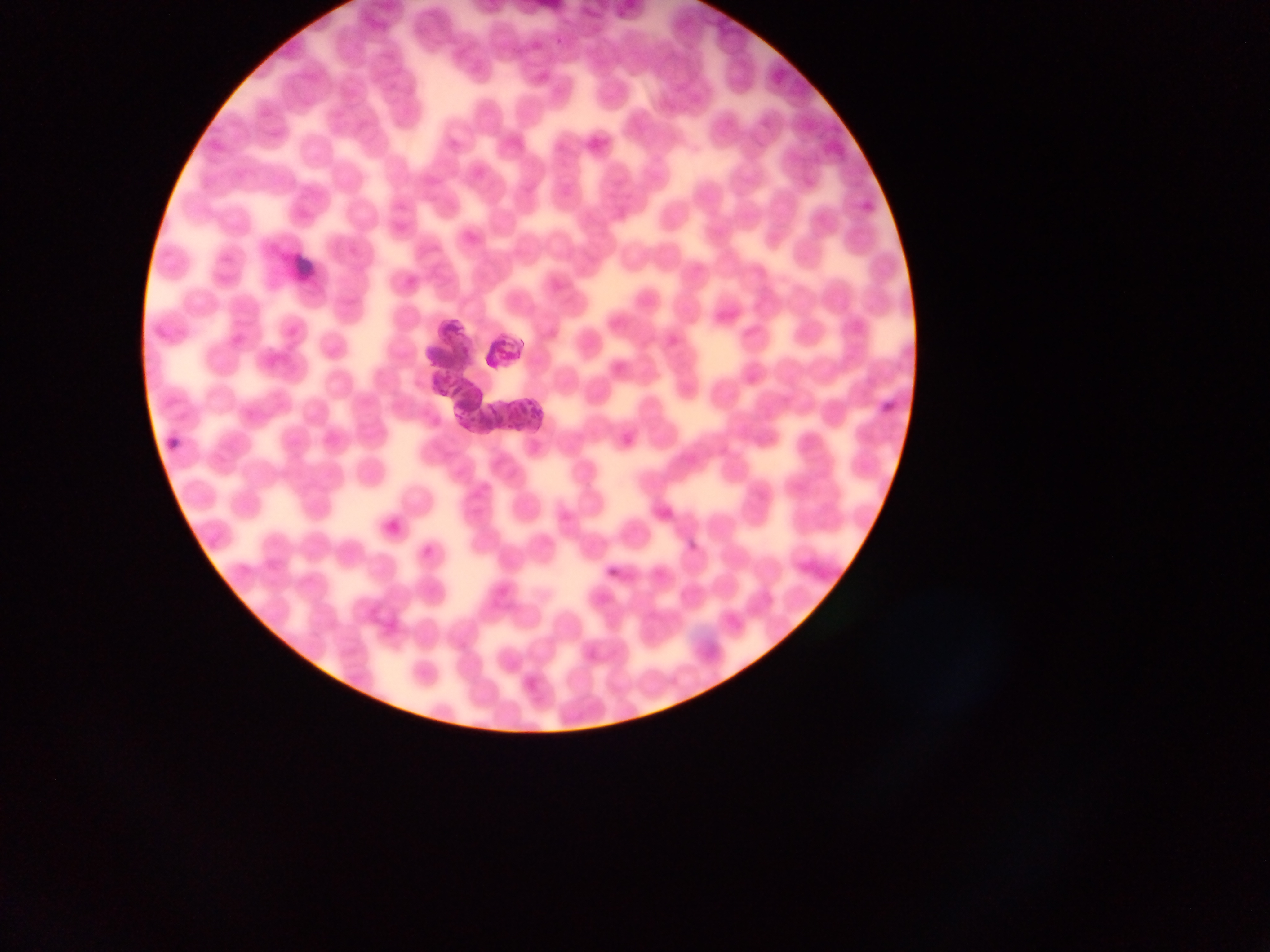
Approximate bounding boxes as (left, top, right, bottom) in pixels. Artifact (stain precipitate or debris) locations: (442, 312, 477, 354). Malaria parasite locations: (510, 350, 518, 358), (527, 396, 537, 406), (489, 402, 498, 415), (520, 407, 529, 416), (532, 409, 546, 417), (508, 423, 515, 432), (519, 423, 527, 431) | approximate (x, y) pixel centers of objects too small to bound: (510, 340), (513, 413). Photographed through a microscope with a mobile-phone camera. Single field of view. Thin blood film. Image is 1270×952 pixels. Sample from Ghana.